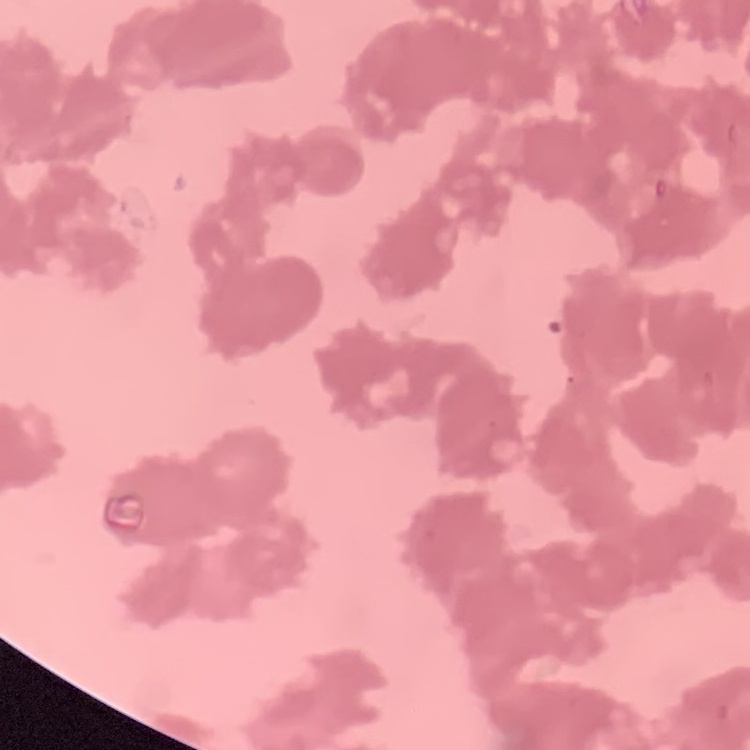

The red blood cells show rouleaux formation. Square crop of a larger photomicrograph. Thin blood smear. Stained with either Field's or Giemsa.